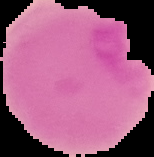
image size = 154×157 pixels
preparation = thin blood smear
result = no Plasmodium parasites seen
image type = segmented cell region with the area outside set to black